Classify this cell by malaria status.
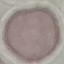
Uninfected.

Thin blood film. Acquired by smartphone through the microscope eyepiece. Automatically extracted cell patch, resized to 64 × 64 pixels. Giemsa-stained preparation.